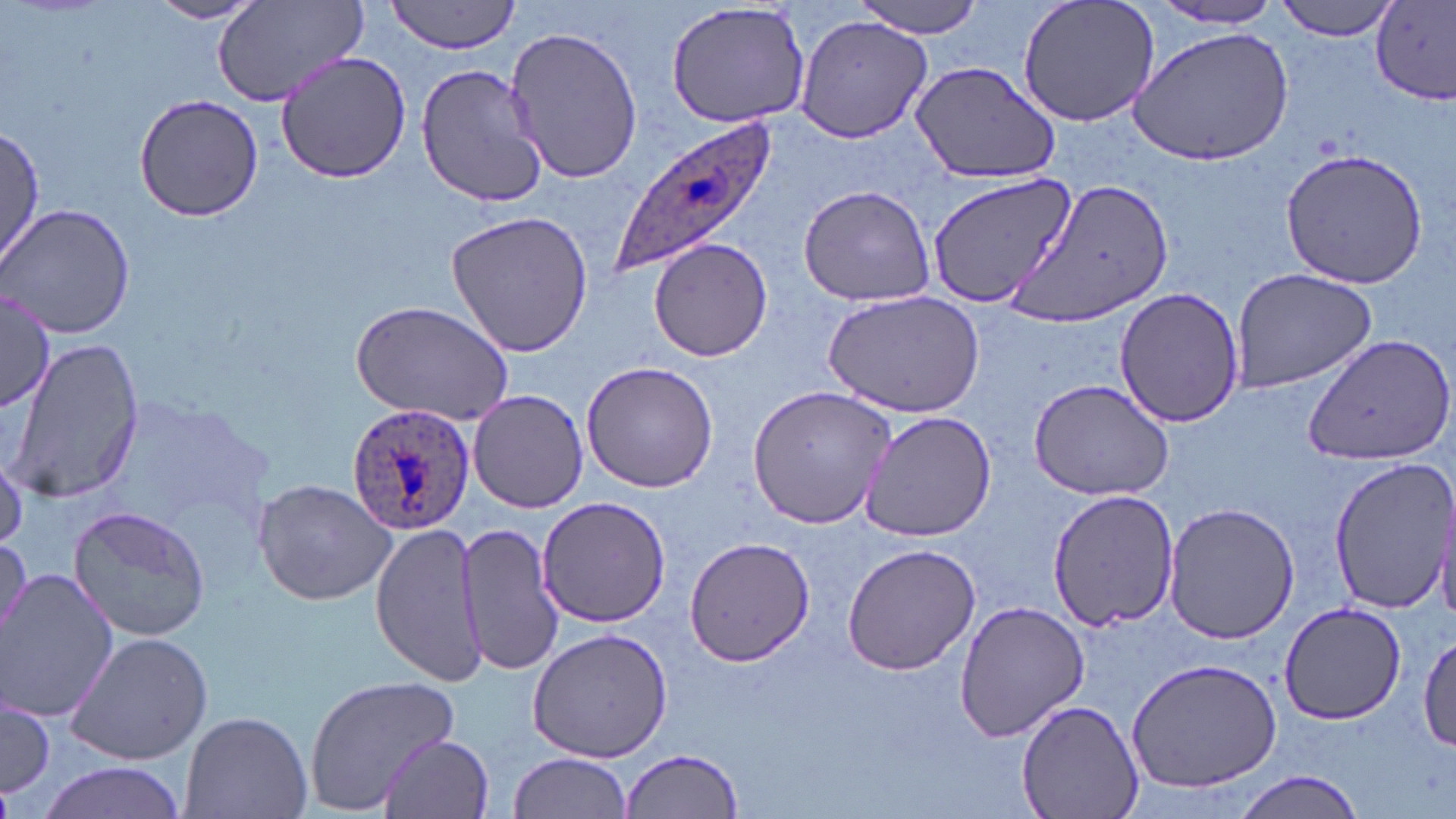

slide-level diagnosis = Plasmodium ovale
field of view = single
modality = optical microscopy
image size = 1456×819 pixels
preparation = thin blood film
stain = May-Grünwald-Giemsa
Plasmodium ovale-infected red blood cell locations = approximate bounding boxes as (x1,y1)-(x2,y2) corner pairs in pixels: (609,118)-(783,278), (347,404)-(477,538)
uninfected red blood cell locations = approximate bounding boxes as (x1,y1)-(x2,y2) corner pairs in pixels: (211,0)-(367,111), (854,0)-(987,39), (1016,0)-(1161,129), (1274,0)-(1400,41), (146,1)-(266,24), (387,1)-(522,54), (665,1)-(814,128), (1148,3)-(1290,30), (1372,3)-(1456,104), (794,15)-(932,141), (505,25)-(643,187), (1131,27)-(1294,163), (275,53)-(411,182), (909,59)-(1063,184), (414,61)-(552,208), (134,95)-(263,222), (0,127)-(46,274), (1281,148)-(1429,289), (927,175)-(1075,309), (1003,176)-(1174,332), (797,184)-(935,307), (1,203)-(135,339), (445,209)-(594,358), (649,238)-(773,362), (1229,266)-(1378,391), (0,285)-(57,417), (1114,286)-(1245,430), (822,291)-(986,419), (350,299)-(516,426), (1301,331)-(1456,467), (7,337)-(146,505), (580,359)-(719,494), (1026,374)-(1176,501), (746,385)-(897,528), (467,389)-(588,513), (861,410)-(999,541), (1327,458)-(1456,615), (254,477)-(400,606), (1048,487)-(1179,630), (536,496)-(673,627), (1163,501)-(1299,644), (67,504)-(211,642), (456,521)-(566,677), (372,523)-(484,686), (0,530)-(30,654), (684,538)-(815,665), (841,541)-(982,676), (2,570)-(117,722), (954,599)-(1091,743), (1280,603)-(1408,725), (525,627)-(673,763), (1419,629)-(1456,753), (63,631)-(211,765), (1125,657)-(1283,794), (303,675)-(460,811), (1,692)-(54,803), (1018,701)-(1142,819), (181,708)-(313,819), (380,732)-(496,819), (621,748)-(746,818), (506,753)-(633,819), (36,761)-(192,819), (1230,770)-(1366,818)
magnification = 1000x